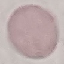

result: negative for malaria parasites
preparation: thin blood smear
image_type: cell patch, automatically extracted from a larger field of view and resized to 64 × 64 pixels
capture: smartphone through the microscope eyepiece
stain: Giemsa